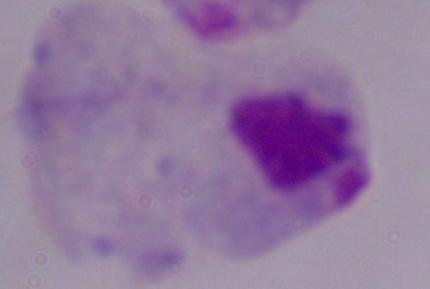 A trichomonad is shown. 1000x magnification. Micrograph.